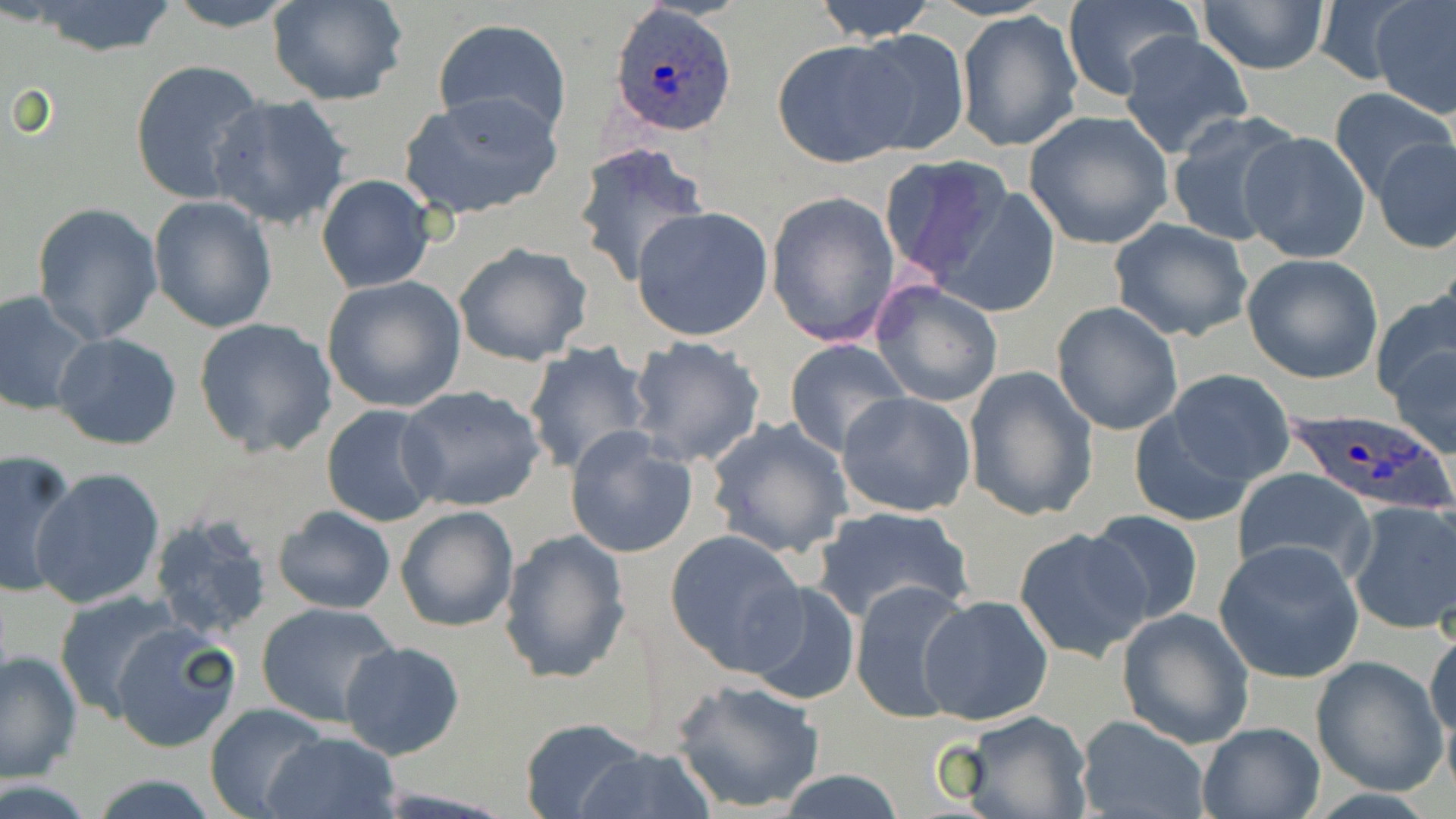

Approximate bounding boxes as (x1, y1, x2, y2) in pixels. Uninfected red blood cell locations: (160, 0, 305, 31), (268, 0, 408, 106), (812, 0, 939, 41), (1312, 1, 1421, 86), (1371, 1, 1456, 118), (25, 2, 179, 57), (1060, 2, 1201, 101), (1196, 2, 1330, 74), (956, 12, 1083, 153), (431, 18, 573, 139), (845, 29, 972, 158), (1119, 32, 1254, 159), (772, 38, 915, 167), (129, 58, 266, 205), (1328, 87, 1455, 200), (400, 90, 562, 220), (205, 93, 354, 231), (1022, 110, 1174, 250), (1164, 111, 1304, 249), (1236, 131, 1372, 265), (1373, 137, 1455, 255), (573, 141, 709, 288), (877, 155, 1013, 285), (316, 174, 436, 293), (929, 184, 1065, 317), (764, 190, 901, 349), (148, 196, 277, 334), (31, 201, 165, 345), (630, 206, 773, 342), (1109, 218, 1254, 342), (453, 241, 593, 367), (1242, 253, 1385, 383), (320, 276, 467, 413), (870, 280, 1004, 408), (1373, 286, 1456, 410), (0, 291, 98, 417), (1050, 301, 1184, 436), (193, 317, 338, 457), (53, 332, 183, 449), (626, 335, 769, 468), (784, 338, 910, 456), (1387, 339, 1456, 459), (521, 341, 653, 475), (962, 365, 1099, 523), (1156, 369, 1293, 490), (396, 384, 548, 511), (837, 391, 980, 518), (1126, 399, 1263, 527), (321, 403, 445, 527), (706, 416, 854, 560), (564, 427, 699, 559), (0, 451, 81, 599), (29, 467, 165, 610), (1231, 468, 1377, 586), (1345, 501, 1456, 636), (273, 504, 397, 615), (395, 504, 520, 633), (811, 504, 972, 626), (1083, 508, 1207, 627), (147, 513, 277, 642), (1014, 526, 1152, 663), (499, 529, 631, 684), (665, 529, 807, 674), (1214, 540, 1366, 683), (850, 579, 976, 728), (741, 581, 862, 706), (54, 590, 186, 721), (919, 593, 1054, 725), (254, 602, 396, 728), (1115, 608, 1254, 749), (108, 623, 242, 753), (1426, 623, 1456, 759), (339, 639, 465, 761), (0, 648, 82, 785), (1310, 655, 1447, 795), (672, 677, 825, 814), (205, 703, 330, 818), (961, 711, 1093, 819), (1075, 715, 1210, 819), (520, 717, 649, 818), (1195, 721, 1325, 818), (266, 729, 399, 819), (573, 745, 715, 818), (774, 770, 910, 819), (89, 775, 224, 817). Plasmodium ovale-infected red blood cell locations: (609, 4, 735, 137), (1285, 407, 1454, 520). Slide-level diagnosis: Plasmodium ovale. Optical microscopy. Thin blood smear. May-Grünwald-Giemsa stain. Single field of view. Image is 1456×819 pixels. 1000x magnification.